Name the parasite shown.
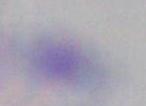

Toxoplasma gondii.

Captured at 1000x magnification. Micrograph.